Name the parasite shown.
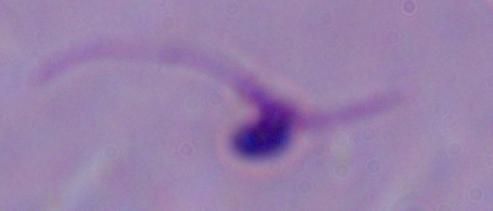

This is Leishmania.

Summary:
  - Modality: photomicrograph
  - Magnification: 1000x